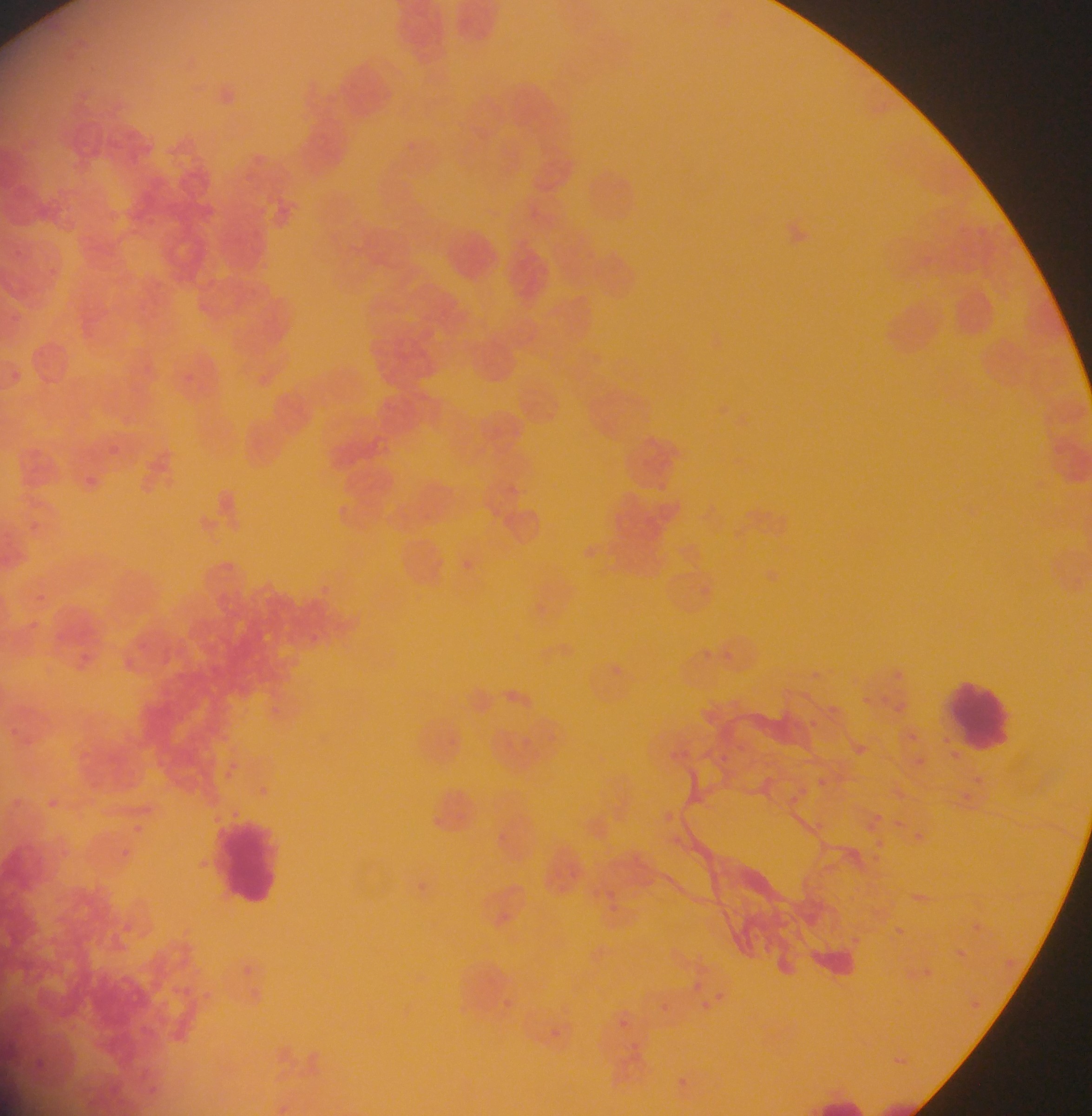

preparation: thin blood smear
country: Ghana
capture: mobile-phone photograph through a microscope
leukocyte_locations: 'approximate bounding boxes as (left, top, right, bottom) in pixels: (941, 670, 1017, 759), (210, 809, 289, 911), (818, 1093, 867, 1116)'
malaria_parasite_locations: 'approximate bounding boxes as (left, top, right, bottom) in pixels: (403, 140, 420, 151), (184, 374, 193, 382), (96, 440, 127, 457), (81, 466, 109, 499), (19, 513, 63, 554), (460, 558, 478, 580), (765, 570, 777, 585), (22, 589, 47, 605), (305, 629, 320, 646), (719, 647, 746, 671), (610, 663, 629, 675), (894, 666, 912, 682), (881, 689, 903, 715), (862, 696, 871, 705), (264, 700, 283, 715), (824, 700, 842, 718), (807, 718, 822, 733), (908, 729, 921, 741), (451, 735, 465, 750), (729, 740, 746, 754), (714, 751, 737, 768), (916, 752, 933, 770), (951, 752, 960, 760), (224, 761, 242, 771), (810, 766, 851, 812), (257, 782, 274, 795), (903, 819, 929, 843), (492, 828, 511, 847), (566, 866, 580, 881), (598, 879, 639, 923), (917, 879, 930, 903), (952, 940, 969, 964), (715, 984, 736, 996), (661, 994, 682, 1019), (973, 994, 991, 1018), (502, 995, 528, 1015), (618, 1019, 628, 1028), (552, 1028, 568, 1044), (678, 1074, 691, 1088)'
image_size: 1092×1116 pixels
field_of_view: single